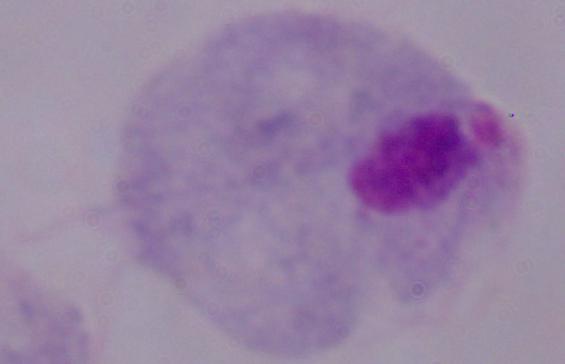 Micrograph. A trichomonad is shown. 1000x magnification.